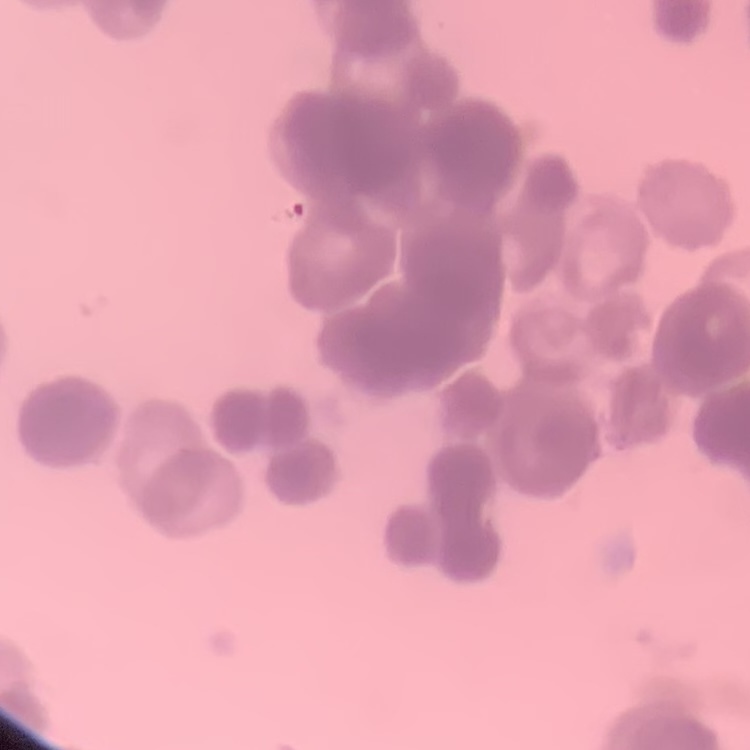 The erythrocytes exhibit rouleaux formation. Stained with either Field's or Giemsa. Thin blood smear. One tile cut from a larger photomicrograph.